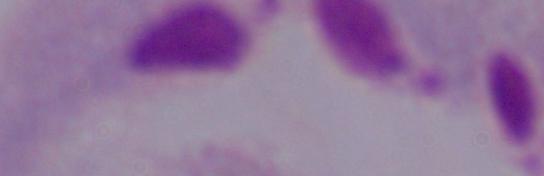
identification = trichomonad
modality = photomicrograph
magnification = 1000x